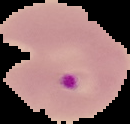

Summary:
  - Image size: 130×124 pixels
  - Image type: segmented cell region on a black background
  - Preparation: thin blood smear
  - Malaria status: parasitized